Name the parasite shown.
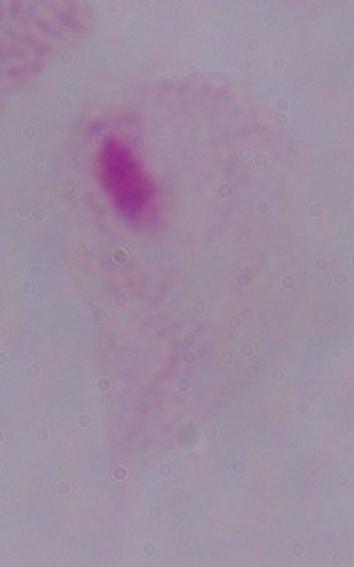

A trichomonad.

Summary:
  - Modality: micrograph
  - Magnification: 1000x